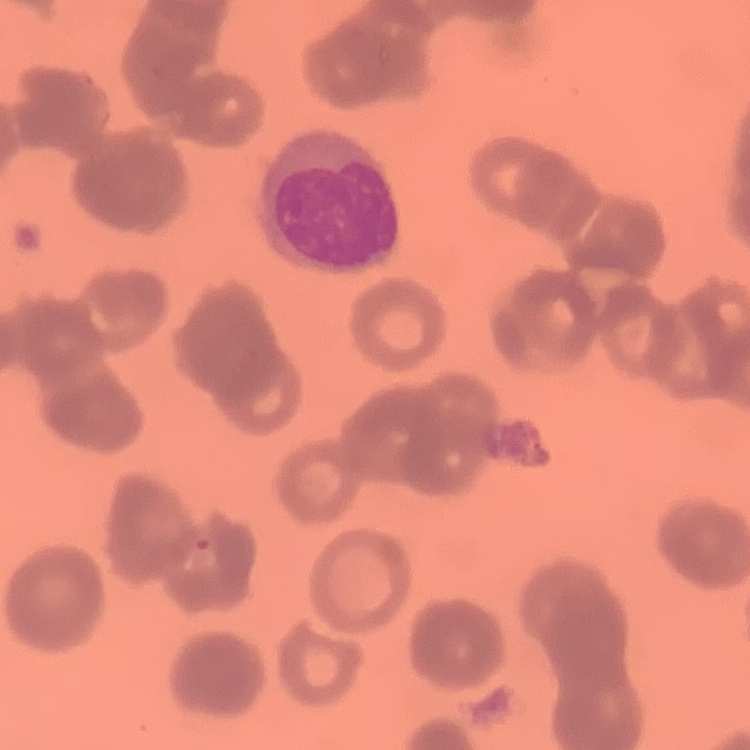

Summary:
  - Red blood cell morphology: rouleaux formation
  - Image type: square crop of a larger photomicrograph
  - Preparation: thin peripheral smear
  - Stain: Field's or Giemsa